State the blood parasite species.
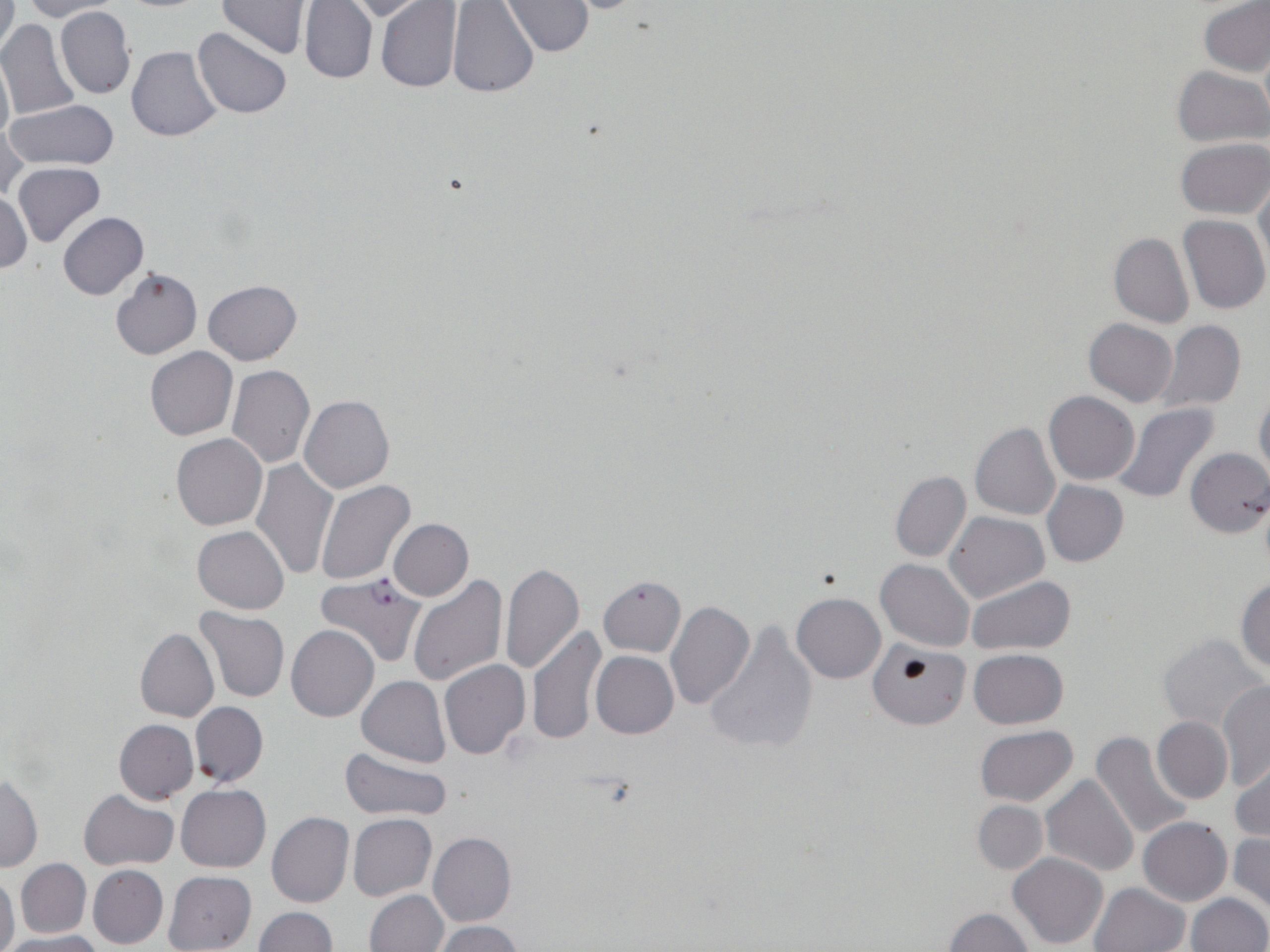

Plasmodium falciparum.

Summary:
  - Coordinate format: approximate bounding boxes as (x1,y1)-(x2,y2) corner pairs in pixels
  - Plasmodium falciparum-infected red blood cell locations: (316,573)-(428,668)
  - Uninfected red blood cell locations: (1,1)-(18,64), (20,1)-(123,21), (215,1)-(314,58), (299,1)-(379,84), (336,1)-(428,22), (447,1)-(541,99), (501,1)-(593,57), (1198,1)-(1270,78), (376,2)-(464,92), (56,5)-(136,99), (0,19)-(81,120), (193,28)-(292,119), (126,46)-(222,141), (0,52)-(13,148), (1173,66)-(1269,148), (3,99)-(121,171), (0,119)-(27,202), (1175,138)-(1268,219), (12,163)-(104,247), (1254,177)-(1270,274), (1,191)-(31,274), (59,212)-(148,299), (1177,215)-(1269,317), (1109,233)-(1194,328), (109,267)-(202,360), (203,279)-(301,365), (1084,318)-(1177,406), (1156,321)-(1247,415), (146,347)-(238,440), (227,365)-(315,468), (1254,389)-(1270,483), (1044,391)-(1139,485), (298,395)-(394,494), (1115,404)-(1219,504), (970,423)-(1061,520), (171,433)-(268,530), (1184,448)-(1270,537), (252,458)-(338,579), (890,471)-(971,562), (315,479)-(416,585), (1042,480)-(1128,566), (945,511)-(1048,603), (389,519)-(473,600), (192,526)-(289,614), (877,559)-(975,652), (500,563)-(584,674), (406,574)-(507,684), (598,576)-(686,657), (967,576)-(1078,655), (1235,576)-(1270,673), (792,592)-(885,683), (665,601)-(755,711), (195,607)-(289,702), (704,621)-(819,756), (286,624)-(380,721), (527,627)-(605,745), (135,628)-(219,723), (1158,634)-(1267,731), (866,640)-(975,735), (968,648)-(1068,729), (591,650)-(679,739), (439,660)-(530,760), (357,675)-(450,768), (1216,681)-(1270,790), (191,702)-(268,787), (1153,717)-(1233,805), (114,719)-(198,804), (974,725)-(1078,806), (1090,730)-(1195,842), (339,747)-(451,822), (1230,757)-(1270,845), (1,774)-(42,872), (1041,774)-(1139,879), (176,784)-(270,871), (80,789)-(178,870), (973,801)-(1048,874), (267,812)-(354,909), (347,814)-(436,900), (1138,817)-(1232,906), (429,832)-(516,926), (1228,832)-(1270,916), (1007,852)-(1109,949), (15,859)-(91,939), (88,865)-(168,948), (163,870)-(257,952), (0,871)-(19,952), (1088,882)-(1190,952), (364,889)-(449,952), (1187,894)-(1268,952), (253,907)-(336,952), (943,907)-(1034,952), (433,921)-(522,952), (3,932)-(105,952)
  - Preparation: thin blood film
  - Field of view: one of a larger specimen
  - Magnification: 1000x
  - Image size: 1270×952 pixels
  - Stain: May-Grünwald-Giemsa
  - Modality: optical microscopy